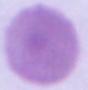
modality = micrograph
identification = red blood cell
magnification = 1000x